Identify the parasite.
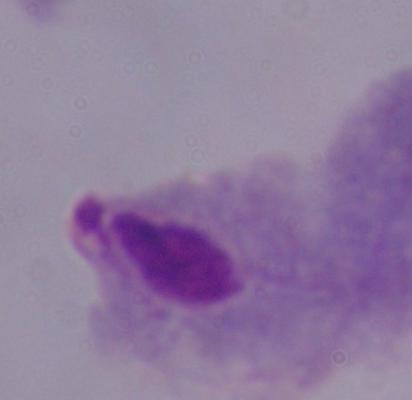
This is a trichomonad.

modality = photomicrograph
magnification = 1000x